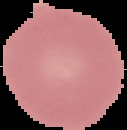

preparation = thin blood smear
image size = 127×130 pixels
image type = cell region segmented out of the field of view; surrounding area masked to black
malaria status = uninfected